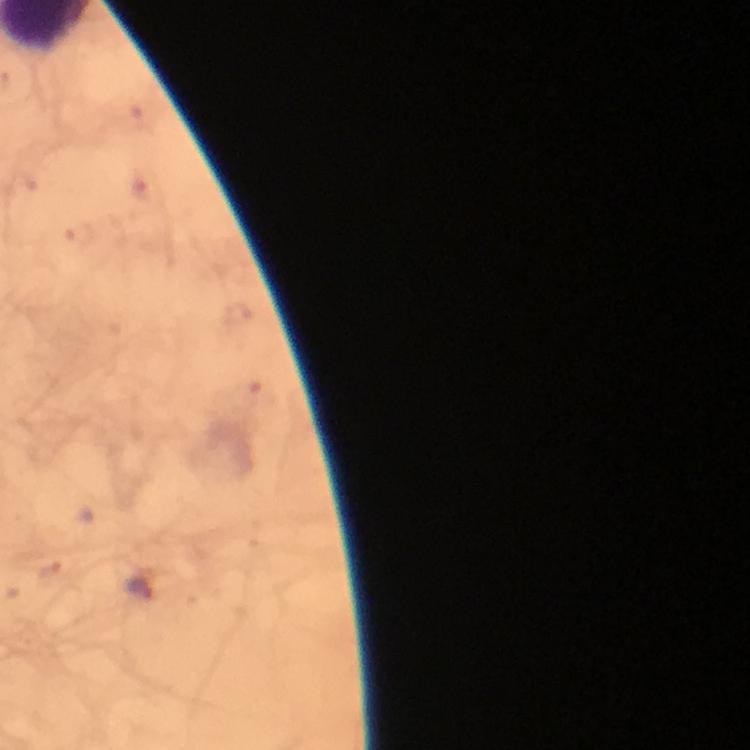

Approximate centers as (x, y) in pixels.
Summary:
  - Plasmodium parasite locations: (139, 587)
  - Immersion oil: applied
  - Stain: Giemsa
  - Image size: 750×750 pixels
  - Cropped from: a single field of view
  - Magnification: 100x
  - Capture: smartphone mounted on the microscope
  - Context: from a malaria diagnostic workup
  - Preparation: thick blood smear